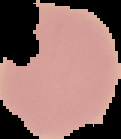

Summary:
  - Image size: 121×139 pixels
  - Image type: cell region segmented out of the field of view; surrounding area masked to black
  - Result: no malaria parasites detected
  - Preparation: thin blood smear